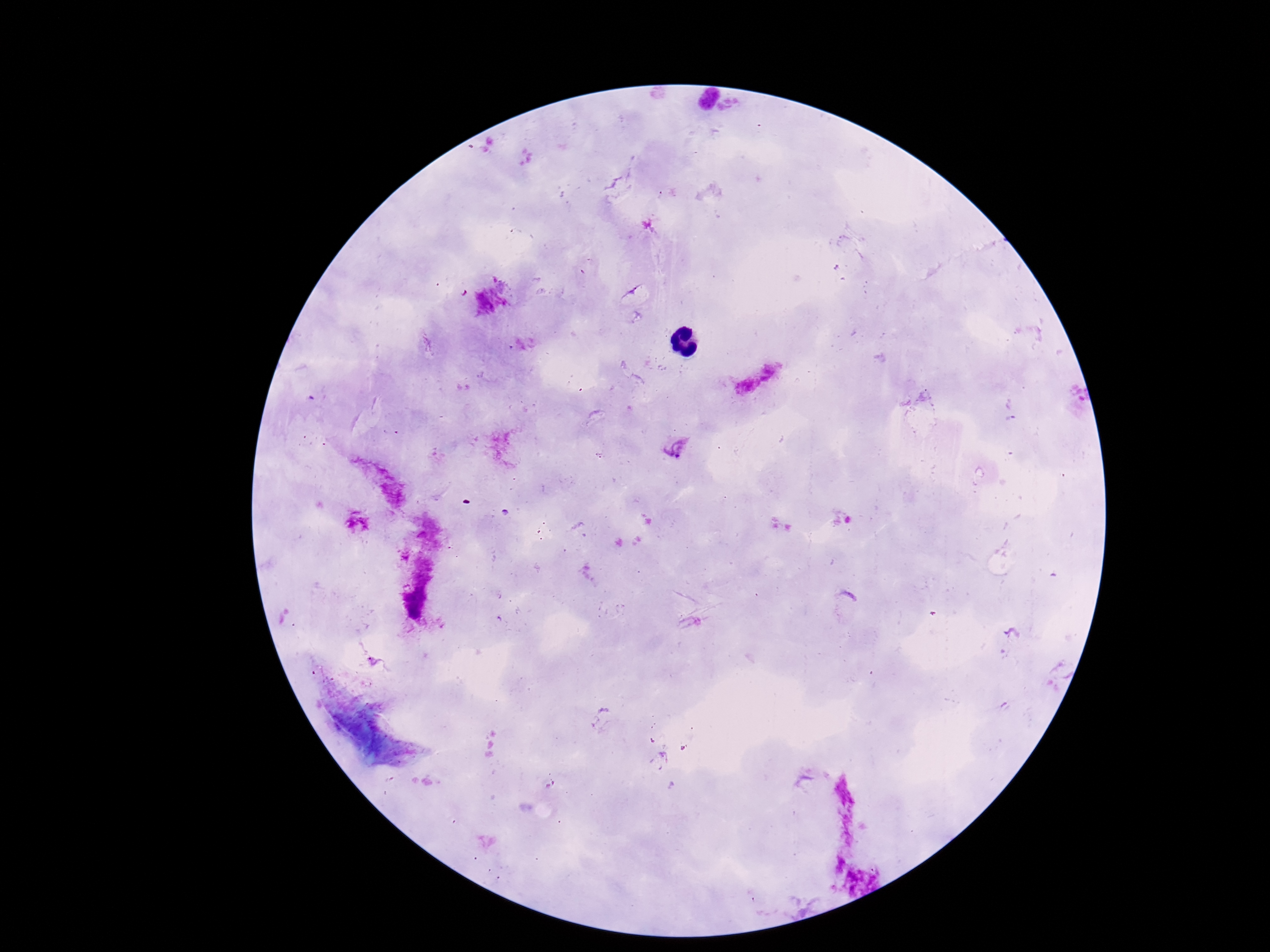

{
  "preparation": "thick peripheral-blood smear",
  "patient_malaria_status": "infected",
  "magnification": "100x",
  "plasmodium_parasite_locations": "approximate centers as {x, y} in pixels: {674, 446}",
  "capture": "smartphone camera through the microscope eyepiece",
  "stain": "Giemsa",
  "image_size": "1270×952 pixels",
  "field_of_view": "one from this slide"
}